Assess this cell for malaria.
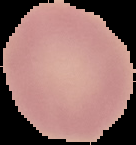
Uninfected.

From a thin blood film. Image is 136×145 pixels. Segmented cell region on a black background.